Classify this cell by malaria status.
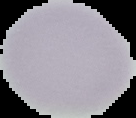
It is uninfected.

{
  "image_type": "segmented cell region with the area outside set to black",
  "image_size": "136×118 pixels",
  "preparation": "thin blood film"
}